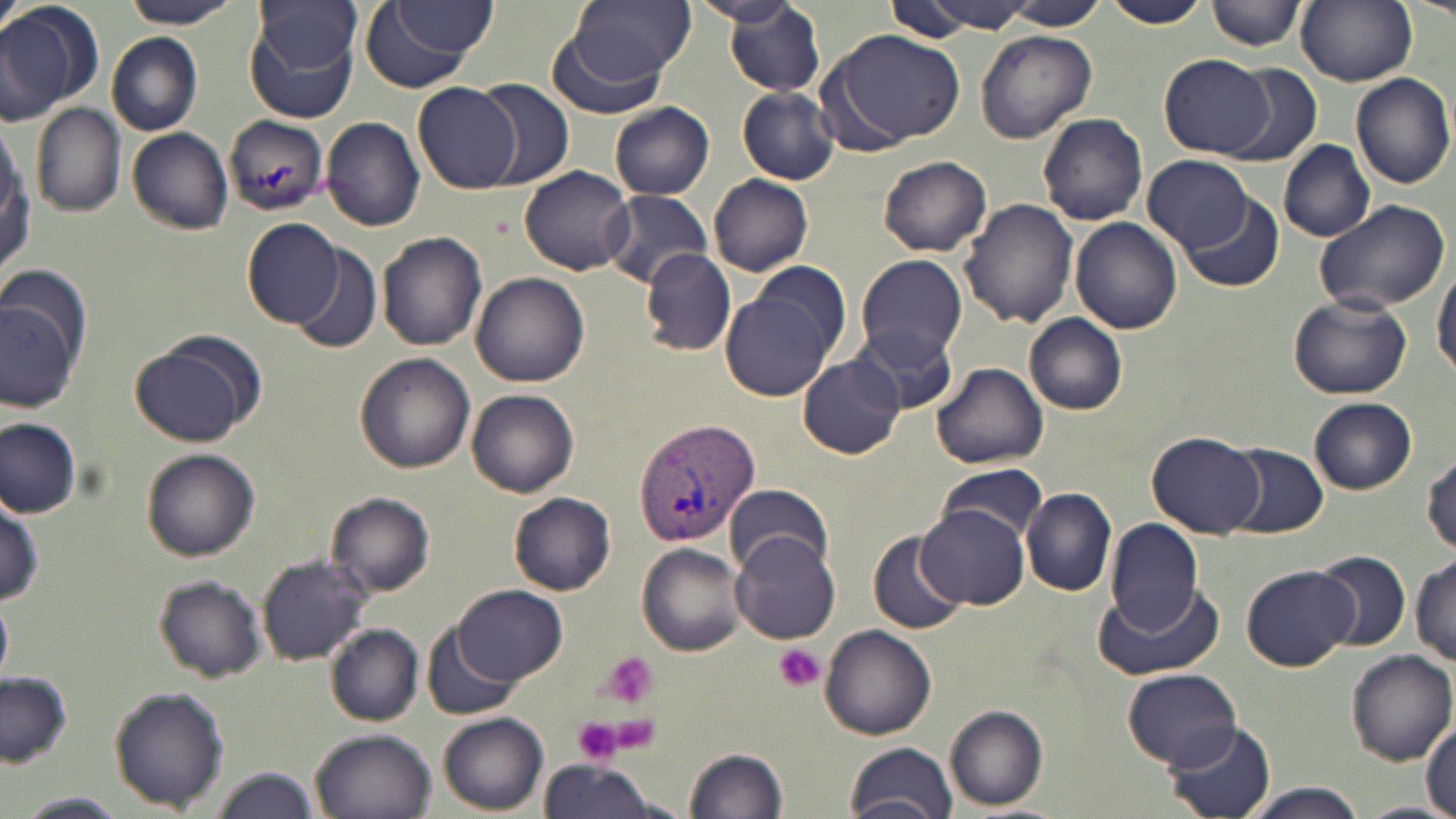
Summary:
  - Coordinate format: approximate bounding boxes as (x1,y1)-(x2,y2) corner pairs in pixels
  - Plasmodium vivax-infected red blood cell locations: (633,417)-(761,546)
  - Platelet locations: (774,644)-(826,693), (599,652)-(660,709), (573,716)-(624,766)
  - Uninfected red blood cell locations: (117,0)-(244,28), (562,0)-(694,86), (698,0)-(802,31), (881,0)-(986,43), (1003,0)-(1107,30), (1102,0)-(1208,28), (1208,0)-(1302,52), (1294,0)-(1417,87), (1409,0)-(1456,21), (0,1)-(100,124), (913,1)-(1034,32), (255,2)-(365,83), (358,3)-(489,91), (721,3)-(826,97), (393,4)-(499,57), (246,24)-(357,123), (547,26)-(678,118), (976,29)-(1096,143), (821,30)-(965,152), (106,31)-(202,136), (1162,54)-(1275,158), (1224,65)-(1322,168), (1349,72)-(1456,189), (474,77)-(575,189), (413,82)-(522,193), (737,87)-(841,184), (609,101)-(715,200), (32,104)-(126,217), (1038,112)-(1149,225), (223,115)-(331,217), (320,116)-(425,232), (0,124)-(35,280), (127,127)-(233,236), (1279,140)-(1376,243), (879,155)-(992,256), (1142,155)-(1253,248), (519,165)-(634,274), (708,174)-(813,276), (601,190)-(715,286), (1183,192)-(1284,292), (959,197)-(1078,329), (1312,198)-(1451,315), (1071,216)-(1184,334), (242,218)-(346,328), (376,230)-(488,351), (289,243)-(383,354), (642,248)-(736,355), (856,254)-(970,364), (1432,266)-(1456,378), (473,273)-(590,388), (719,278)-(844,402), (0,286)-(84,414), (1287,292)-(1414,400), (1025,314)-(1129,415), (851,326)-(959,414), (128,334)-(260,449), (356,354)-(476,474), (797,355)-(904,458), (932,362)-(1048,470), (466,388)-(579,496), (1309,398)-(1417,493), (0,417)-(80,519), (1145,430)-(1267,539), (1226,442)-(1329,538), (141,448)-(261,562), (1423,448)-(1456,557), (937,461)-(1050,546), (724,483)-(832,577), (1021,486)-(1117,597), (508,490)-(616,596), (1,492)-(44,608), (325,492)-(434,598), (918,506)-(1031,609), (1102,517)-(1205,633), (869,533)-(966,637), (731,534)-(841,646), (635,543)-(747,657), (1311,550)-(1410,652), (1411,553)-(1456,667), (257,554)-(373,666), (1243,563)-(1357,670), (153,576)-(265,683), (1093,582)-(1228,682), (453,584)-(565,685), (0,600)-(11,679), (326,624)-(425,724), (423,624)-(521,721), (822,624)-(936,739), (1344,650)-(1456,765), (1123,669)-(1242,769), (0,670)-(72,766), (109,686)-(229,810), (944,705)-(1049,812), (438,712)-(549,814), (1165,721)-(1277,819), (1422,721)-(1456,815), (309,727)-(438,819), (844,742)-(959,819), (684,746)-(788,818), (538,760)-(660,819), (209,766)-(320,819), (1242,784)-(1369,819), (18,792)-(128,817)
  - Slide-level diagnosis: Plasmodium vivax
  - Magnification: 1000x
  - Modality: optical microscopy
  - Stain: May-Grünwald-Giemsa
  - Preparation: thin blood smear
  - Field of view: single
  - Image size: 1456×819 pixels